Classify this cell by malaria status.
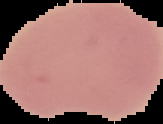
Uninfected.

Summary:
  - Preparation: thin blood smear
  - Image type: segmented cell region on a black background
  - Image size: 163×124 pixels